Name the cell type shown.
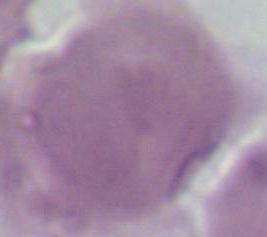
This is an erythrocyte.

Summary:
  - Modality: micrograph
  - Magnification: 1000x